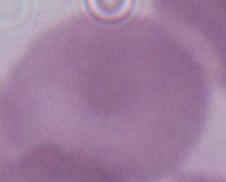
identification = erythrocyte
modality = photomicrograph
magnification = 1000x